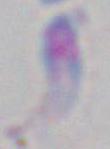

Captured at 1000x magnification. Micrograph. Toxoplasma gondii is shown.